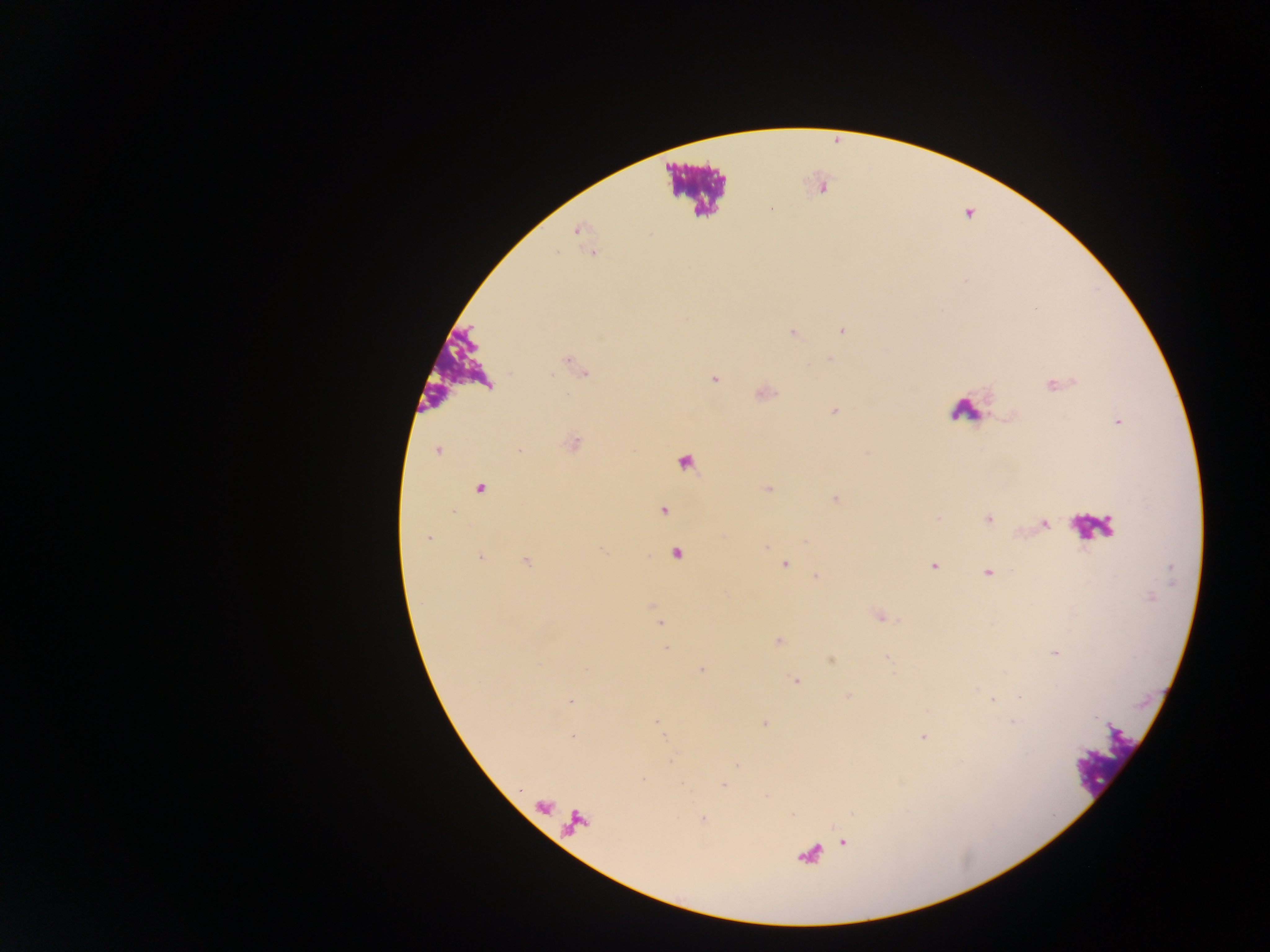
Approximate centers as x y in pixels.
Summary:
  - Malaria parasite locations: 821 186; 772 209; 577 229; 592 252; 841 330; 792 332; 829 359; 567 361; 583 372; 714 379; 1052 384; 762 392; 834 410; 1117 421; 571 443; 438 449; 685 462; 479 487; 766 488; 836 498; 663 510; 939 518; 987 519; 1044 524; 428 537; 601 549; 677 553; 479 558; 526 561; 785 564; 933 566; 987 573; 815 577; 653 605; 879 615; 661 623; 778 641; 667 647; 1055 653; 887 657; 831 660; 701 669; 796 679; 847 695; 1020 696; 571 701; 656 722; 765 723; 573 736; 923 737; 723 784; 543 805; 702 819; 843 842
  - Leukocyte locations: 697 189; 458 368; 965 410; 1092 527; 1104 761
  - Country: Ghana
  - Image size: 1270×952 pixels
  - Preparation: thick blood smear
  - Capture: mobile-phone photograph through a microscope
  - Field of view: single